Locate every malaria parasite.
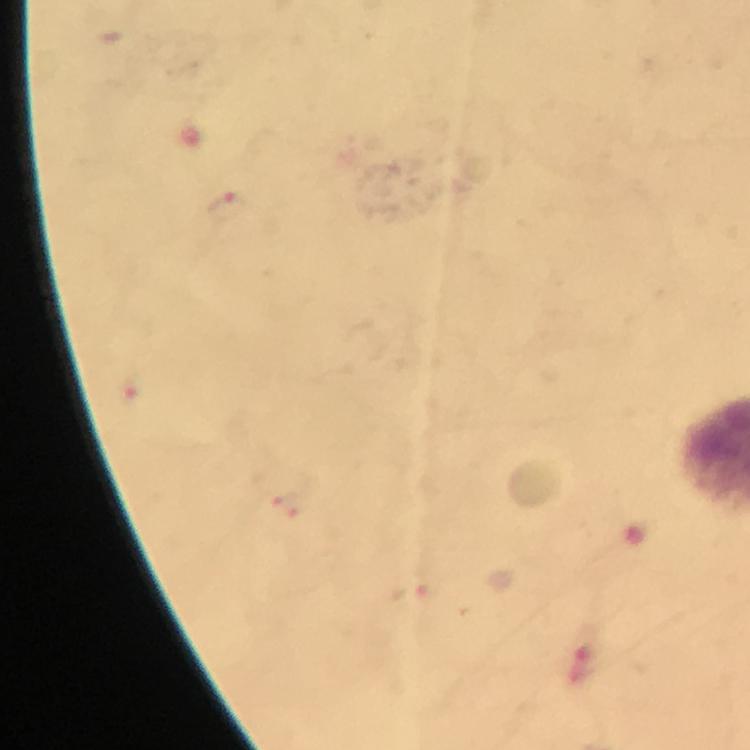

Approximate centers as [x, y] in pixels.
Malaria parasites: [227, 207], [289, 506], [415, 599].

{
  "capture": "smartphone photograph through a microscope",
  "context": "from a diagnostic examination for malaria",
  "image_size": "750×750 pixels",
  "magnification": "100x",
  "preparation": "thick blood smear",
  "immersion_oil": "applied",
  "cropped_from": "a single field of view",
  "stain": "Giemsa"
}